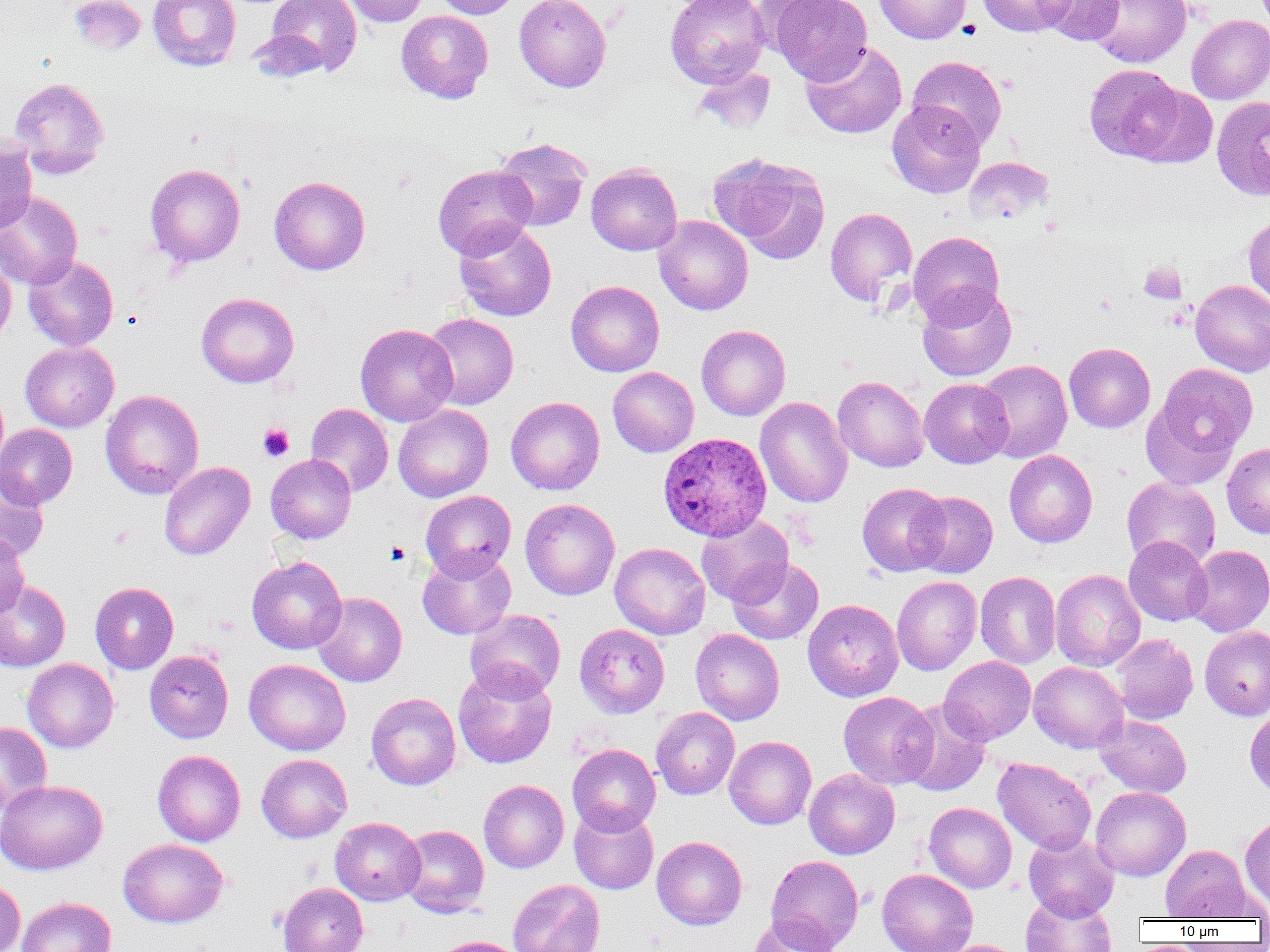

Approximate bounding boxes as (x1, y1, x2, y2) in pixels. Uninfected red blood cell locations: (68, 0, 146, 55), (148, 0, 241, 70), (265, 0, 361, 75), (339, 0, 429, 27), (432, 0, 523, 19), (514, 0, 611, 92), (665, 0, 770, 88), (768, 0, 872, 85), (874, 0, 971, 44), (977, 0, 1076, 36), (1037, 0, 1124, 46), (1088, 0, 1192, 68), (396, 10, 493, 103), (1186, 14, 1270, 104), (246, 29, 329, 83), (801, 41, 907, 139), (907, 56, 1007, 150), (1084, 64, 1185, 162), (693, 65, 776, 135), (9, 77, 109, 179), (1131, 83, 1218, 169), (1210, 95, 1270, 202), (886, 101, 985, 198), (0, 138, 37, 235), (494, 138, 592, 231), (709, 154, 830, 262), (964, 156, 1054, 224), (586, 163, 682, 255), (145, 164, 246, 268), (433, 164, 537, 259), (269, 176, 370, 275), (0, 191, 82, 290), (825, 207, 917, 306), (1243, 214, 1270, 307), (653, 215, 753, 315), (454, 220, 556, 322), (908, 231, 1004, 326), (0, 254, 16, 346), (22, 254, 119, 351), (1190, 279, 1270, 377), (566, 280, 665, 377), (917, 284, 1016, 382), (196, 292, 299, 388), (422, 313, 518, 410), (355, 323, 458, 427), (696, 325, 790, 421), (20, 341, 119, 432), (1064, 342, 1155, 433), (976, 359, 1073, 463), (1145, 363, 1257, 483), (608, 367, 699, 457), (833, 376, 929, 473), (920, 378, 1013, 468), (100, 390, 204, 499), (505, 396, 605, 495), (754, 397, 853, 508), (305, 404, 393, 497), (393, 405, 493, 502), (0, 424, 77, 509), (1222, 443, 1270, 538), (1004, 450, 1098, 548), (265, 454, 356, 544), (158, 462, 255, 561), (0, 470, 49, 562), (1122, 477, 1221, 569), (857, 482, 950, 576), (420, 491, 516, 580), (912, 492, 998, 578), (520, 498, 620, 600), (696, 514, 794, 606), (0, 533, 30, 622), (1124, 536, 1213, 626), (609, 542, 710, 640), (1185, 545, 1270, 637), (417, 549, 516, 640), (247, 556, 347, 654), (727, 557, 824, 645), (1050, 569, 1145, 672), (975, 571, 1061, 668), (892, 576, 981, 675), (0, 580, 71, 672), (90, 582, 178, 674), (312, 591, 407, 687), (802, 599, 904, 702), (464, 609, 566, 700), (575, 624, 670, 718), (1199, 625, 1270, 721), (691, 629, 784, 725), (1111, 634, 1198, 725), (145, 650, 233, 743), (939, 656, 1036, 745), (22, 658, 119, 753), (244, 659, 351, 756), (1028, 661, 1129, 753), (453, 663, 557, 769), (838, 691, 937, 788), (366, 692, 460, 790), (899, 700, 991, 797), (651, 707, 740, 800), (1244, 708, 1270, 798), (1095, 715, 1192, 798), (0, 720, 52, 815), (724, 735, 816, 829), (567, 743, 661, 835), (152, 750, 245, 846), (257, 753, 352, 842), (993, 757, 1096, 855), (803, 768, 900, 859), (0, 779, 107, 875), (478, 780, 569, 872), (1090, 786, 1191, 881), (924, 802, 1017, 893), (569, 805, 659, 895), (1240, 812, 1270, 913), (330, 817, 425, 905), (398, 824, 489, 917), (1023, 833, 1120, 921), (651, 836, 747, 930), (118, 838, 227, 928), (1160, 844, 1251, 921), (765, 854, 864, 952), (876, 868, 978, 952), (0, 879, 25, 952), (507, 879, 605, 952), (277, 882, 368, 952), (1020, 895, 1116, 952), (16, 896, 117, 952), (748, 914, 841, 952), (431, 935, 524, 952), (938, 939, 1026, 952). Platelet locations: (1138, 261, 1186, 304), (257, 424, 294, 462), (109, 525, 134, 548). Plasmodium ovale-infected red blood cell locations: (657, 432, 772, 540). Slide-level diagnosis: Plasmodium ovale. Thin blood film. Optical microscopy. Image is 1270×952 pixels. Single field of view. 1000x magnification.